State the preparation type.
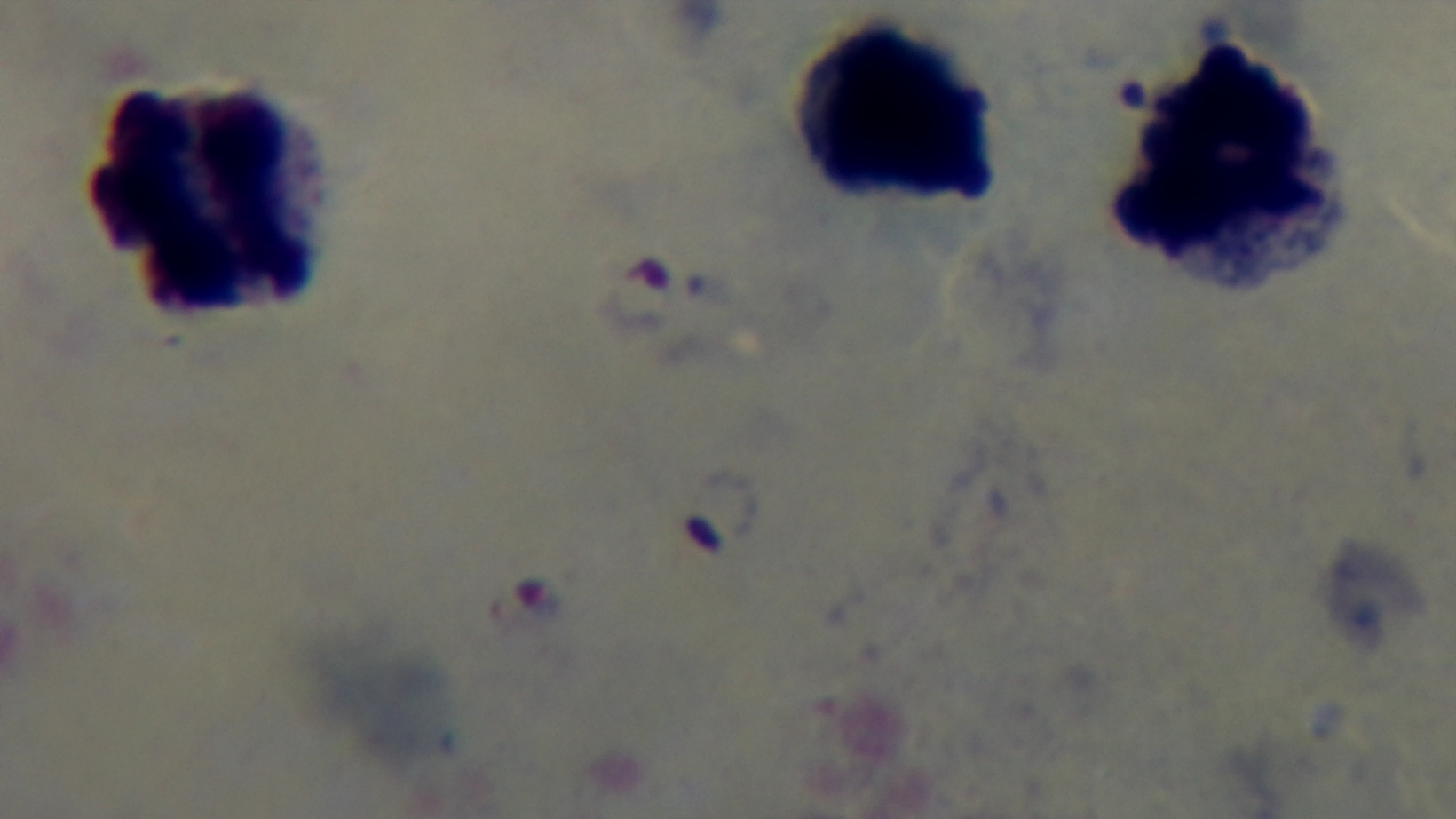
A thick smear.

Summary:
  - Field of view: one from the slide
  - Malaria status: infected
  - Modality: light microscopy
  - Capture: mounted 4K digital camera
  - Objective: 100x oil immersion
  - Stain: Giemsa